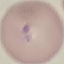

result = malaria parasites identified
stain = Giemsa
preparation = thin blood film
image type = automatically extracted cell patch, resized to 64 × 64 pixels
capture = smartphone camera at the microscope eyepiece